State the preparation type.
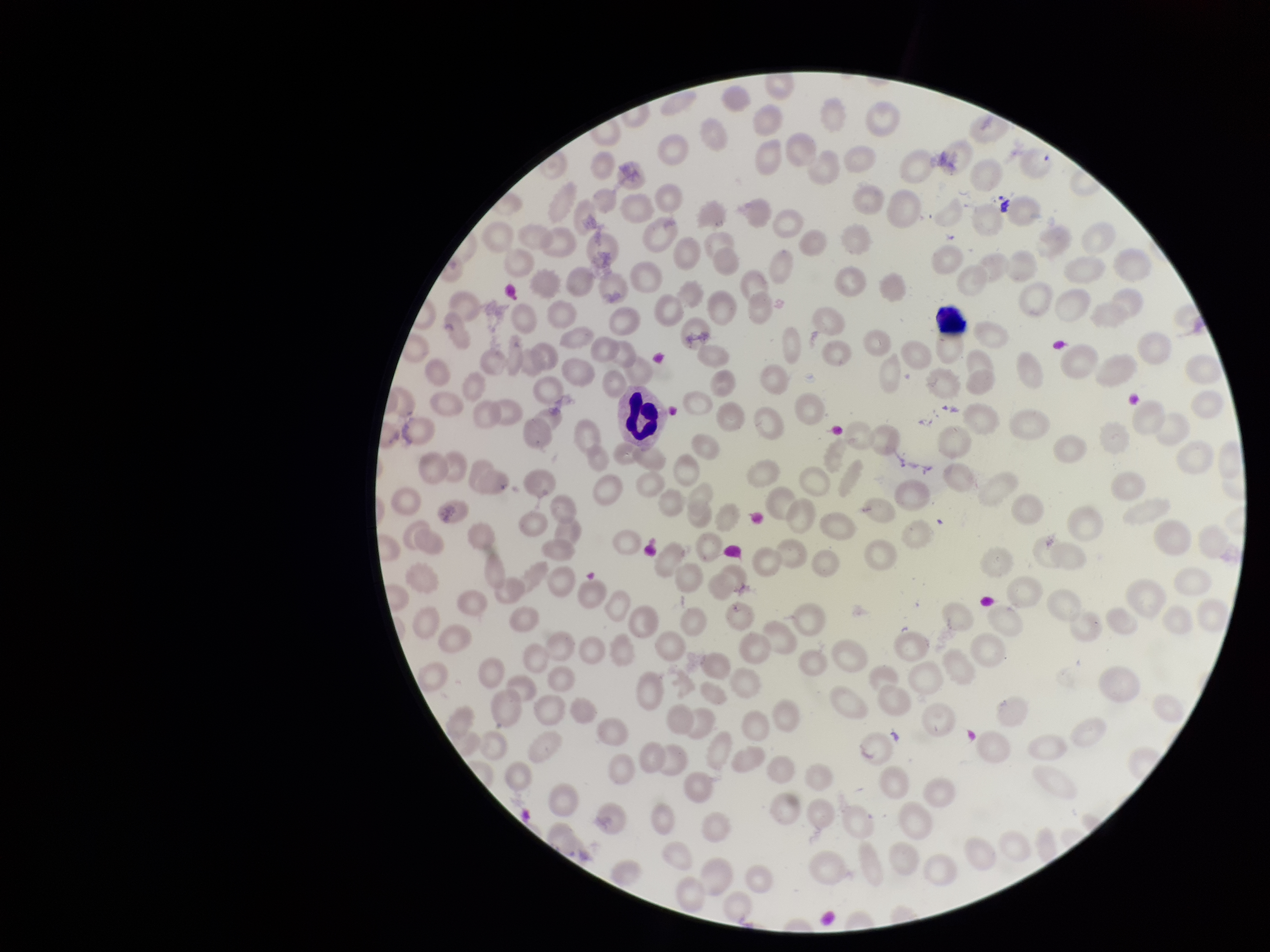
A thin smear.

Summary:
  - Field of view: one from this slide
  - Stain: Giemsa
  - Capture: smartphone photograph through the microscope eyepiece
  - Parasitized red blood cell count: 0
  - Patient malaria status: positive
  - Parasitized red blood cells: none detected
  - Image size: 1270×952 pixels
  - Species reported for this patient: Plasmodium falciparum
  - Red blood cell count: 179